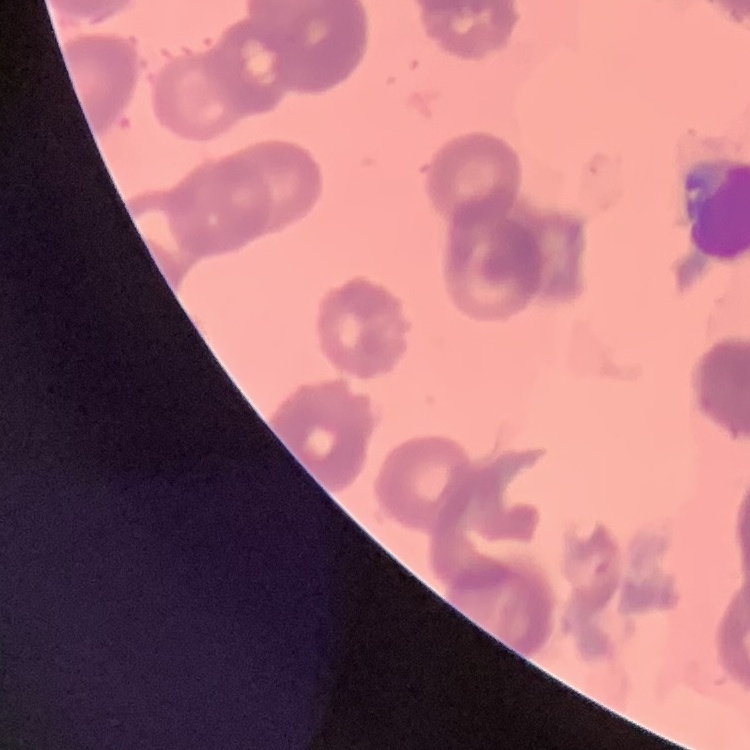

Summary:
  - Erythrocyte morphology: rouleaux formation
  - Stain: Field's or Giemsa
  - Preparation: thin peripheral smear
  - Image type: one tile cut from a larger photomicrograph